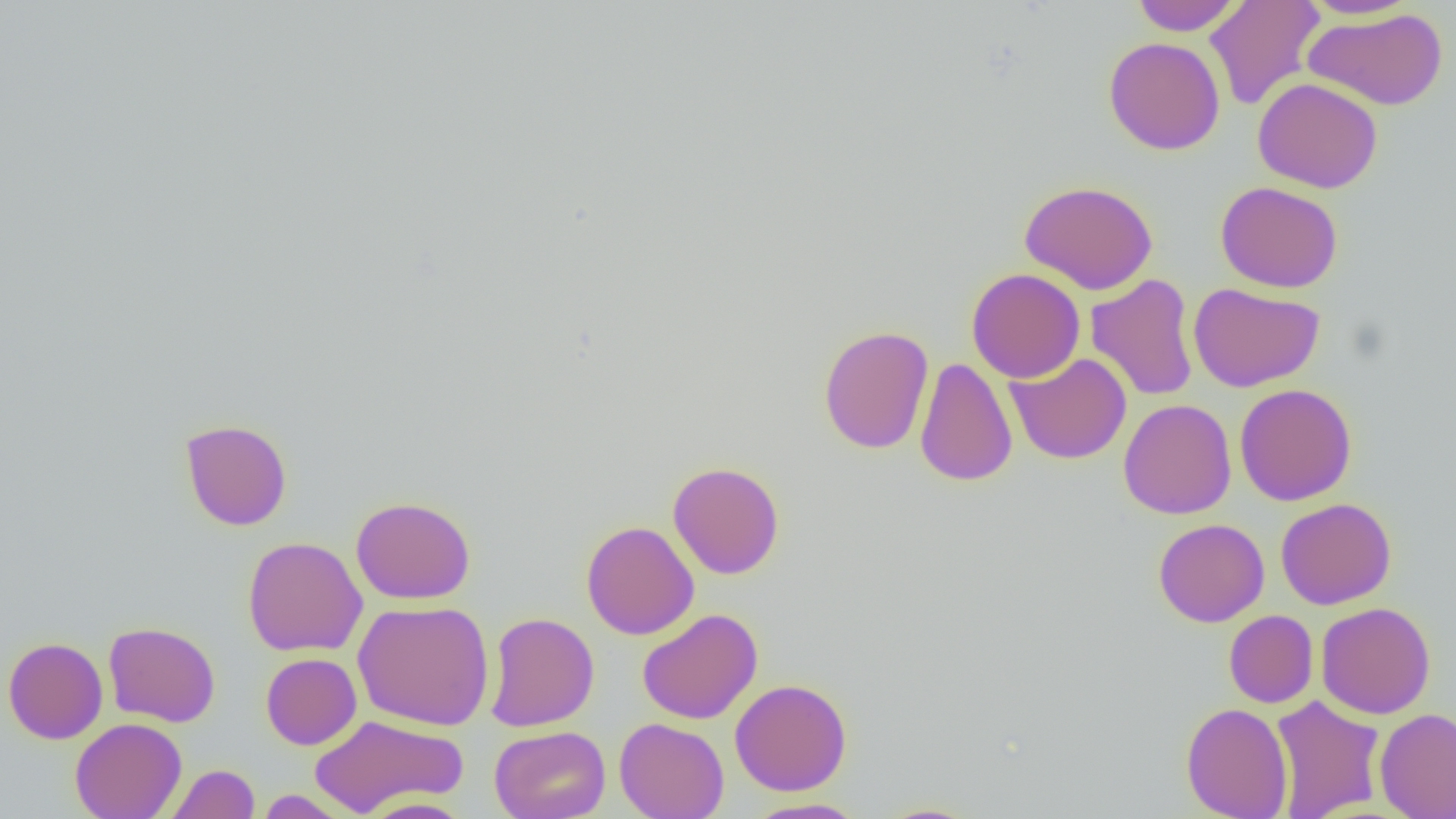
Approximate bounding boxes as [x1, y1, x2, y2] in pixels. Uninfected red blood cell locations: [1131, 0, 1242, 36], [1204, 0, 1325, 111], [1298, 0, 1420, 20], [1304, 8, 1448, 111], [1103, 36, 1225, 155], [1253, 78, 1383, 193], [1019, 180, 1158, 295], [1215, 181, 1344, 293], [966, 268, 1085, 383], [1085, 273, 1200, 402], [1188, 282, 1325, 392], [818, 325, 934, 455], [1005, 353, 1132, 464], [914, 356, 1018, 487], [1234, 384, 1357, 506], [1119, 399, 1237, 519], [180, 418, 292, 531], [667, 461, 785, 579], [350, 495, 476, 605], [1275, 498, 1396, 609], [1153, 518, 1269, 627], [580, 520, 699, 640], [242, 536, 368, 657], [352, 600, 494, 730], [1316, 602, 1436, 719], [637, 608, 762, 724], [1224, 610, 1319, 708], [484, 612, 598, 731], [103, 621, 221, 728], [2, 637, 108, 744], [260, 652, 361, 750], [730, 678, 852, 796], [1270, 695, 1386, 819], [1180, 702, 1293, 819], [1374, 707, 1456, 819], [309, 714, 467, 816], [614, 717, 729, 819], [70, 718, 186, 819], [489, 725, 610, 819], [166, 763, 260, 819], [255, 790, 353, 818], [360, 796, 474, 819], [743, 797, 868, 818], [871, 802, 985, 818]. Slide-level diagnosis: no evidence of blood parasites. Light microscopy. One field of a larger specimen. Thin blood smear. Captured at 1000x magnification. Image is 1456×819 pixels.